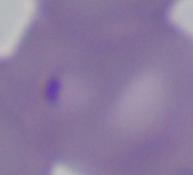

modality = micrograph
magnification = 1000x
identification = Babesia